Point out each leukocyte.
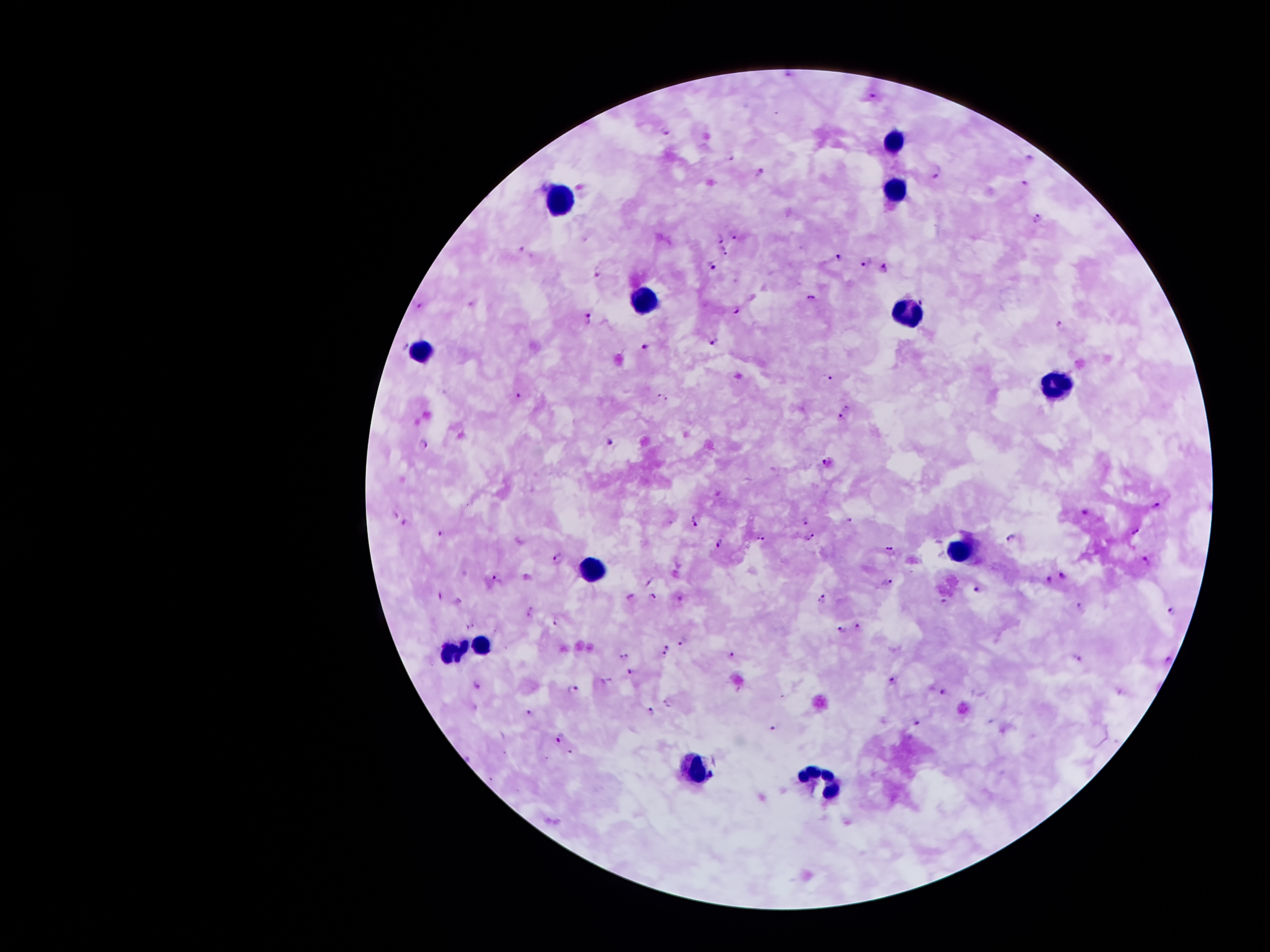
Approximate centers as (x, y) in pixels.
Leukocytes: (895, 140), (895, 188), (558, 199), (643, 303), (905, 312), (419, 350), (1058, 384), (958, 550), (593, 570), (447, 647), (478, 647), (693, 768), (819, 780).

Malaria parasite locations: (788, 73), (873, 97), (667, 130), (732, 155), (1029, 157), (937, 171), (760, 172), (1027, 183), (1039, 218), (733, 232), (721, 239), (522, 249), (725, 251), (838, 257), (866, 262), (714, 265), (884, 269), (599, 270), (811, 298), (921, 302), (419, 305), (735, 309), (588, 317), (1062, 324), (713, 339), (406, 345), (647, 346), (829, 379), (518, 396), (664, 396), (847, 408), (840, 417), (610, 442), (423, 445), (826, 461), (1156, 505), (1085, 513), (396, 514), (850, 519), (695, 520), (403, 521), (806, 522), (1136, 532), (440, 534), (1011, 536), (761, 537), (810, 537), (720, 543), (889, 551), (559, 561), (1144, 562), (1049, 576), (1061, 576), (497, 577), (887, 583), (978, 592), (654, 595), (441, 596), (680, 599), (821, 600), (457, 601), (944, 602), (1082, 607), (1172, 611), (531, 612), (557, 619), (470, 626), (857, 627), (841, 630), (681, 642), (668, 646), (734, 653), (665, 654), (623, 655), (1079, 658), (1170, 658), (629, 669), (892, 681), (476, 682), (573, 690), (944, 692), (530, 711), (652, 713), (917, 724), (773, 727), (560, 735). Giemsa-stained preparation. One field from this slide. 100x magnification. Patient malaria status: infected with Plasmodium falciparum. Smartphone photograph taken through the microscope eyepiece. Thick blood smear. Image is 1270×952 pixels.